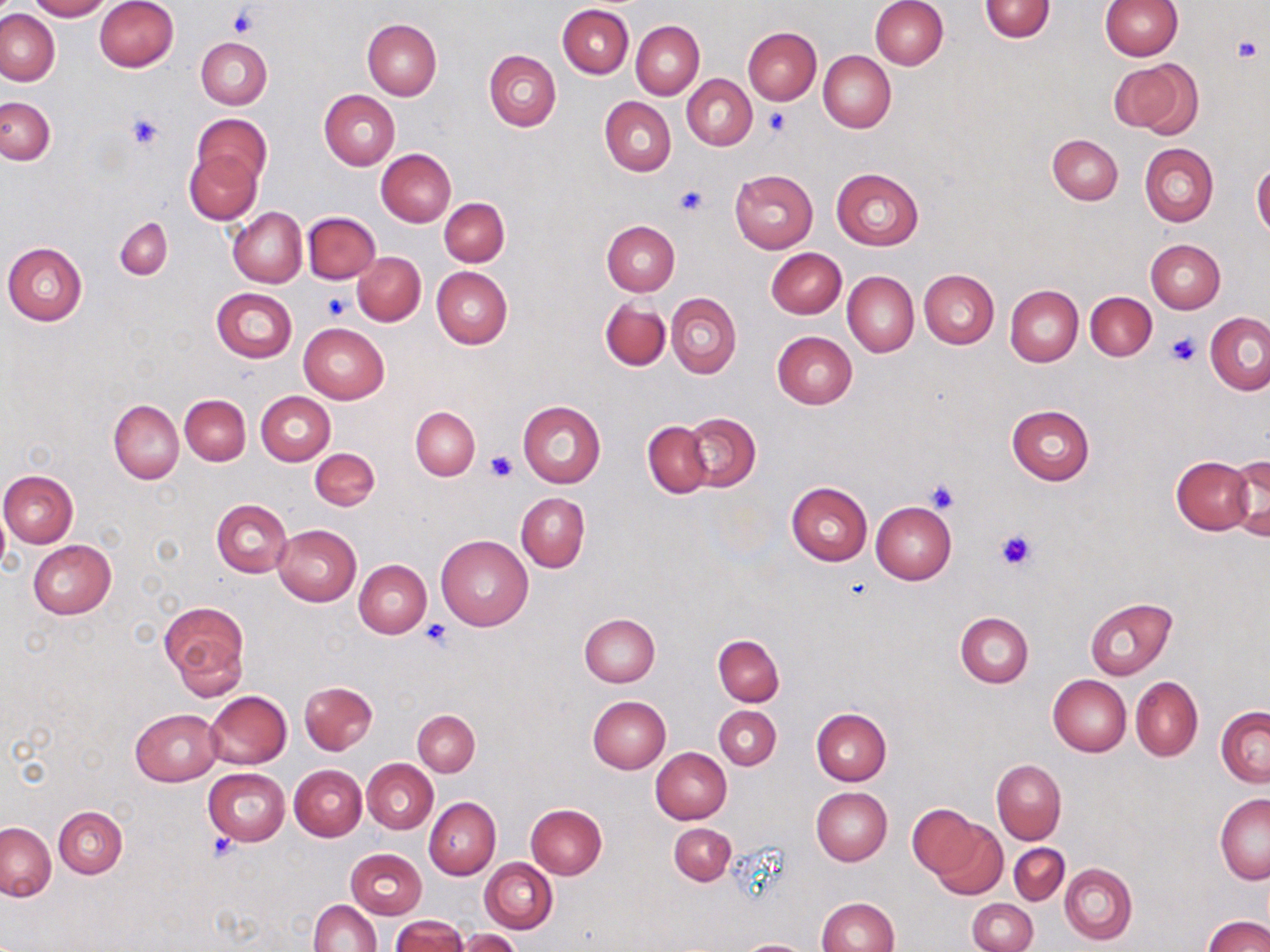
Summary:
  - Coordinate format: approximate bounding boxes as (x1, y1, x2, y2) in pixels
  - Uninfected red blood cell locations: (26, 0, 110, 20), (94, 0, 178, 72), (870, 0, 948, 69), (1100, 0, 1181, 59), (980, 1, 1055, 42), (558, 4, 634, 78), (1, 9, 59, 85), (362, 19, 442, 99), (632, 20, 704, 99), (743, 27, 821, 104), (196, 37, 272, 110), (484, 49, 561, 132), (818, 51, 895, 132), (1109, 58, 1200, 136), (682, 74, 756, 150), (319, 90, 400, 171), (600, 96, 676, 176), (0, 97, 54, 165), (194, 113, 271, 187), (1047, 134, 1122, 205), (1140, 143, 1219, 227), (184, 148, 263, 225), (375, 148, 455, 226), (1252, 163, 1270, 238), (729, 169, 819, 253), (830, 169, 923, 250), (440, 198, 509, 267), (228, 206, 306, 288), (303, 211, 381, 283), (115, 218, 171, 280), (603, 220, 679, 296), (1146, 239, 1225, 313), (2, 242, 88, 325), (767, 247, 845, 318), (354, 252, 424, 325), (432, 266, 512, 348), (919, 269, 999, 348), (842, 271, 919, 357), (1004, 284, 1083, 367), (211, 287, 297, 362), (1085, 291, 1157, 361), (667, 293, 740, 378), (599, 298, 670, 372), (1205, 312, 1270, 395), (299, 323, 389, 403), (771, 331, 857, 409), (256, 391, 335, 465), (180, 394, 250, 466), (108, 400, 183, 482), (517, 400, 605, 488), (1006, 405, 1094, 486), (410, 406, 479, 480), (683, 412, 761, 492), (643, 420, 712, 497), (310, 448, 380, 511), (1227, 453, 1270, 541), (1171, 456, 1253, 534), (1, 470, 77, 548), (786, 482, 872, 566), (516, 493, 589, 572), (211, 499, 291, 577), (870, 501, 957, 584), (273, 525, 361, 605), (435, 534, 533, 630), (27, 539, 116, 619), (354, 559, 431, 637), (1085, 597, 1177, 679), (160, 601, 250, 698), (580, 612, 661, 687), (956, 612, 1033, 687), (714, 635, 784, 706), (1048, 675, 1131, 756), (1131, 676, 1203, 762), (299, 681, 376, 754), (205, 690, 292, 768), (588, 695, 671, 774), (714, 706, 781, 769), (1216, 707, 1270, 787), (130, 709, 221, 785), (412, 709, 479, 776), (812, 709, 891, 786), (651, 747, 732, 824), (363, 759, 438, 833), (991, 760, 1065, 844), (290, 764, 367, 841), (202, 767, 290, 845), (811, 787, 892, 866), (1215, 792, 1270, 884), (425, 797, 501, 879), (526, 803, 607, 879), (907, 804, 986, 880), (53, 807, 127, 878), (931, 820, 1007, 899), (0, 822, 55, 900), (669, 823, 735, 884), (1010, 843, 1068, 906), (346, 847, 427, 919), (480, 858, 558, 933), (1060, 863, 1137, 945), (818, 896, 898, 951), (309, 898, 381, 952), (968, 898, 1037, 952), (391, 915, 468, 952), (1203, 915, 1270, 952), (458, 929, 523, 952), (739, 940, 808, 952)
  - Platelet locations: (228, 8, 258, 36), (1233, 37, 1264, 64), (764, 109, 791, 136), (126, 112, 163, 149), (674, 185, 707, 217), (324, 291, 351, 319), (1167, 333, 1199, 365), (486, 450, 519, 481), (924, 479, 960, 513), (993, 528, 1038, 571), (420, 618, 452, 648), (209, 832, 240, 859)
  - Slide-level diagnosis: no evidence of blood parasites
  - Magnification: 1000x
  - Modality: optical microscopy
  - Field of view: single
  - Preparation: thin blood film
  - Image size: 1270×952 pixels
  - Stain: May-Grünwald-Giemsa